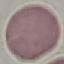
result = no malaria parasites seen
image type = automatically extracted cell patch, resized to 64 × 64 pixels
capture = smartphone camera at the microscope eyepiece
preparation = thin blood film
stain = Giemsa